Give the preparation type.
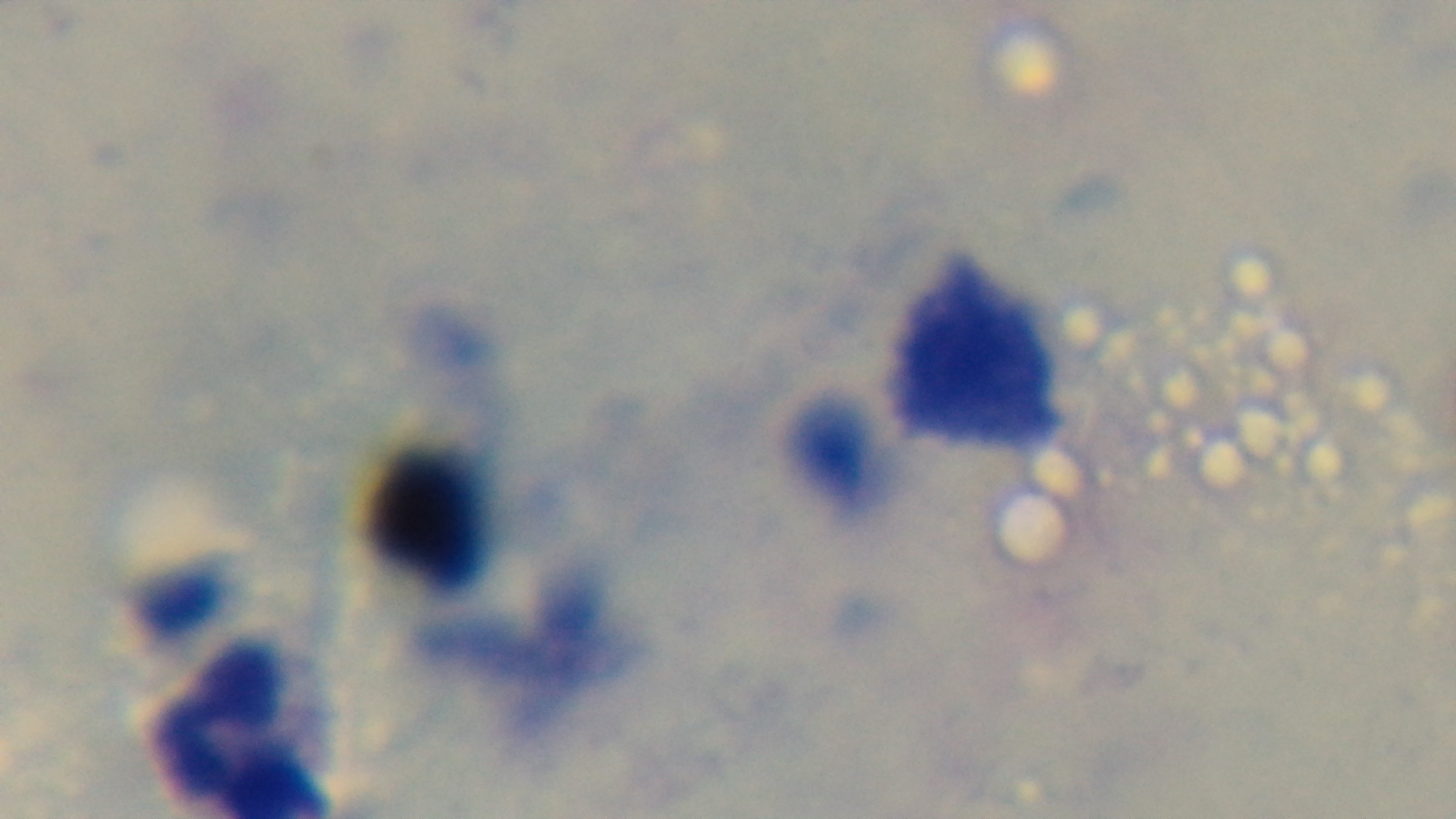

Thick.

modality = light microscopy
field of view = single
malaria status = uninfected
capture = mounted 4K digital camera
stain = Giemsa
objective = 100x oil immersion